Locate and identify every blood parasite.
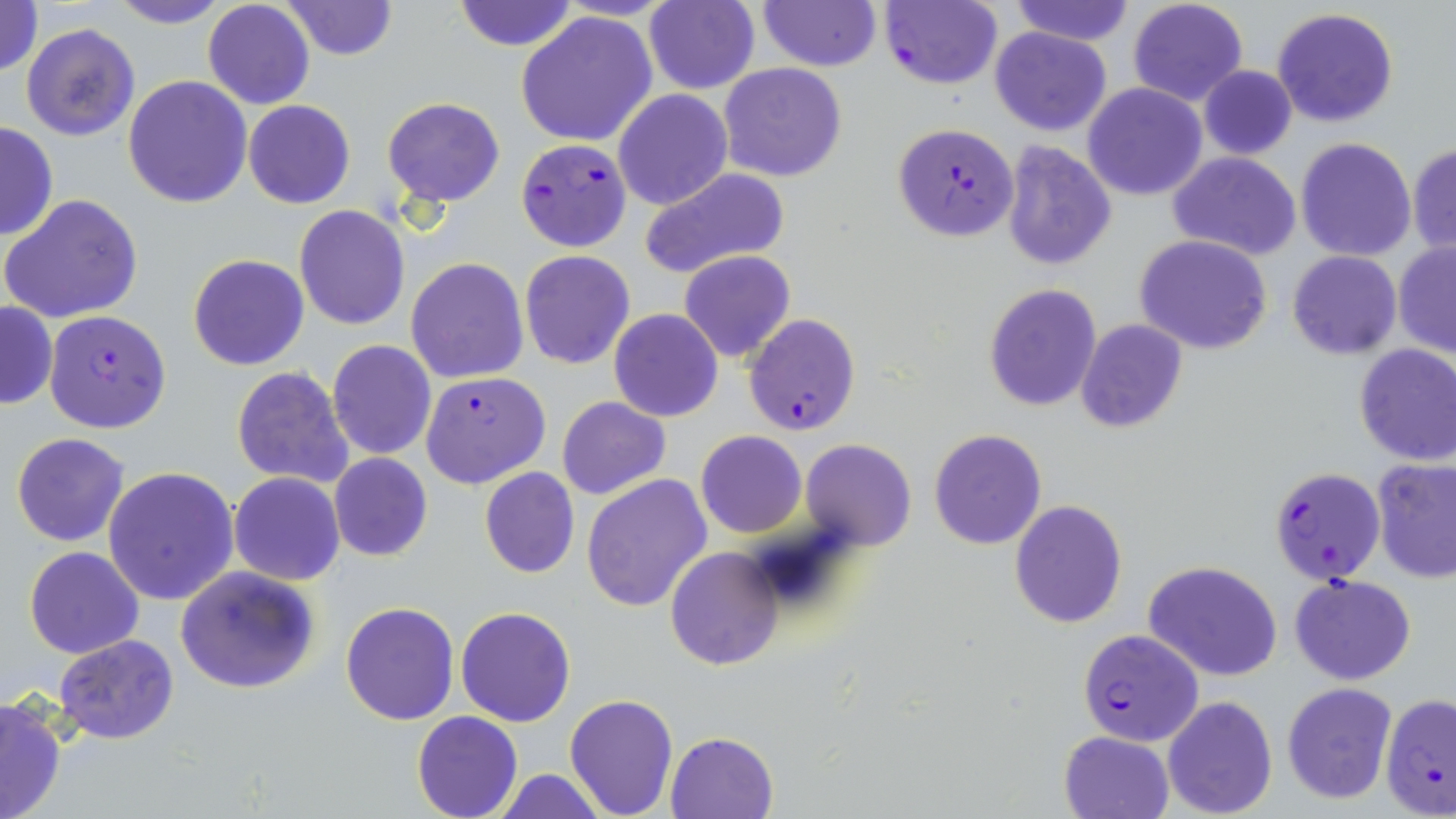
Approximate bounding boxes as [x1, y1, x2, y2] in pixels.
Plasmodium falciparum-infected red blood cells: [880, 0, 1002, 90], [891, 123, 1019, 241], [516, 139, 632, 252], [44, 310, 173, 434], [744, 312, 863, 435], [419, 370, 550, 489], [1270, 466, 1386, 585], [1080, 628, 1203, 741].
No Plasmodium ovale, Plasmodium malariae, Plasmodium vivax, Babesia divergens, or Trypanosoma brucei observed.

Summary:
  - Uninfected red blood cell locations: [0, 0, 44, 80], [107, 0, 230, 28], [451, 0, 577, 51], [644, 0, 758, 94], [757, 0, 882, 71], [1009, 0, 1134, 45], [1127, 0, 1248, 106], [203, 1, 315, 110], [280, 1, 399, 61], [1271, 8, 1399, 128], [514, 10, 659, 148], [20, 22, 142, 142], [990, 26, 1111, 135], [718, 62, 847, 182], [1198, 67, 1297, 159], [123, 75, 253, 210], [1082, 83, 1208, 200], [612, 89, 733, 211], [383, 97, 505, 205], [243, 100, 355, 209], [0, 121, 58, 242], [1295, 137, 1416, 261], [1000, 141, 1117, 271], [1408, 142, 1455, 254], [1167, 151, 1303, 261], [639, 169, 791, 281], [1, 193, 143, 324], [294, 205, 410, 331], [1134, 235, 1274, 355], [1393, 241, 1456, 357], [519, 249, 636, 370], [679, 249, 796, 364], [1287, 250, 1401, 359], [188, 253, 310, 372], [406, 257, 529, 384], [983, 283, 1102, 412], [1, 301, 57, 409], [609, 308, 723, 422], [1075, 319, 1188, 432], [327, 339, 438, 460], [1353, 345, 1456, 466], [231, 366, 354, 490], [557, 397, 671, 501], [929, 428, 1047, 549], [695, 430, 806, 538], [11, 433, 128, 546], [801, 438, 915, 552], [329, 452, 435, 561], [1372, 458, 1456, 584], [101, 466, 239, 605], [480, 467, 580, 578], [228, 472, 345, 585], [582, 475, 713, 613], [1009, 499, 1127, 629], [23, 545, 144, 659], [665, 547, 783, 671], [1143, 559, 1283, 681], [175, 564, 321, 694], [1291, 574, 1416, 685], [341, 600, 459, 725], [456, 606, 576, 727], [55, 634, 180, 744], [1281, 682, 1397, 803], [1379, 692, 1456, 819], [564, 693, 679, 818], [1, 695, 67, 819], [1162, 695, 1278, 819], [411, 710, 523, 819], [1059, 730, 1172, 819], [665, 732, 780, 819], [493, 769, 610, 818]
  - Slide-level diagnosis: Plasmodium falciparum
  - Modality: light microscopy
  - Image size: 1456×819 pixels
  - Field of view: one of a larger specimen
  - Magnification: 1000x
  - Preparation: thin blood film
  - Stain: May-Grünwald-Giemsa